State which parasite is depicted.
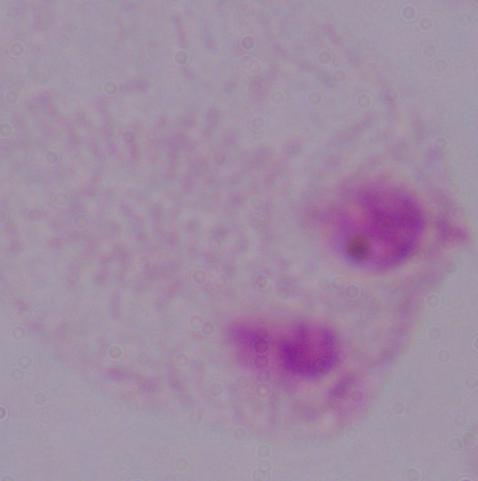

This is a trichomonad.

Summary:
  - Magnification: 1000x
  - Modality: photomicrograph